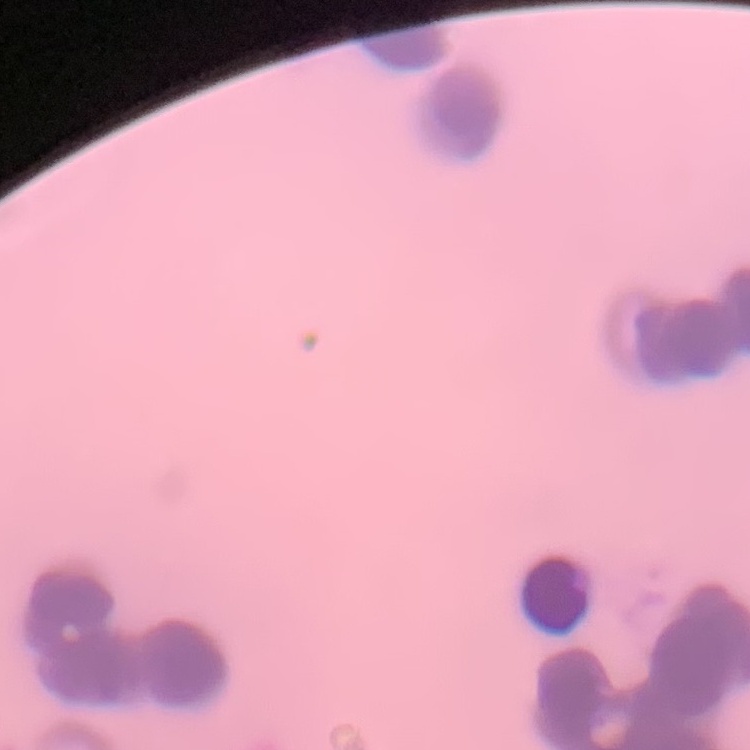

red_blood_cell_morphology: rouleaux formation
preparation: thin blood smear
stain: Field's or Giemsa
image_type: square crop of a larger photomicrograph